Locate every blood parasite and identify its species.
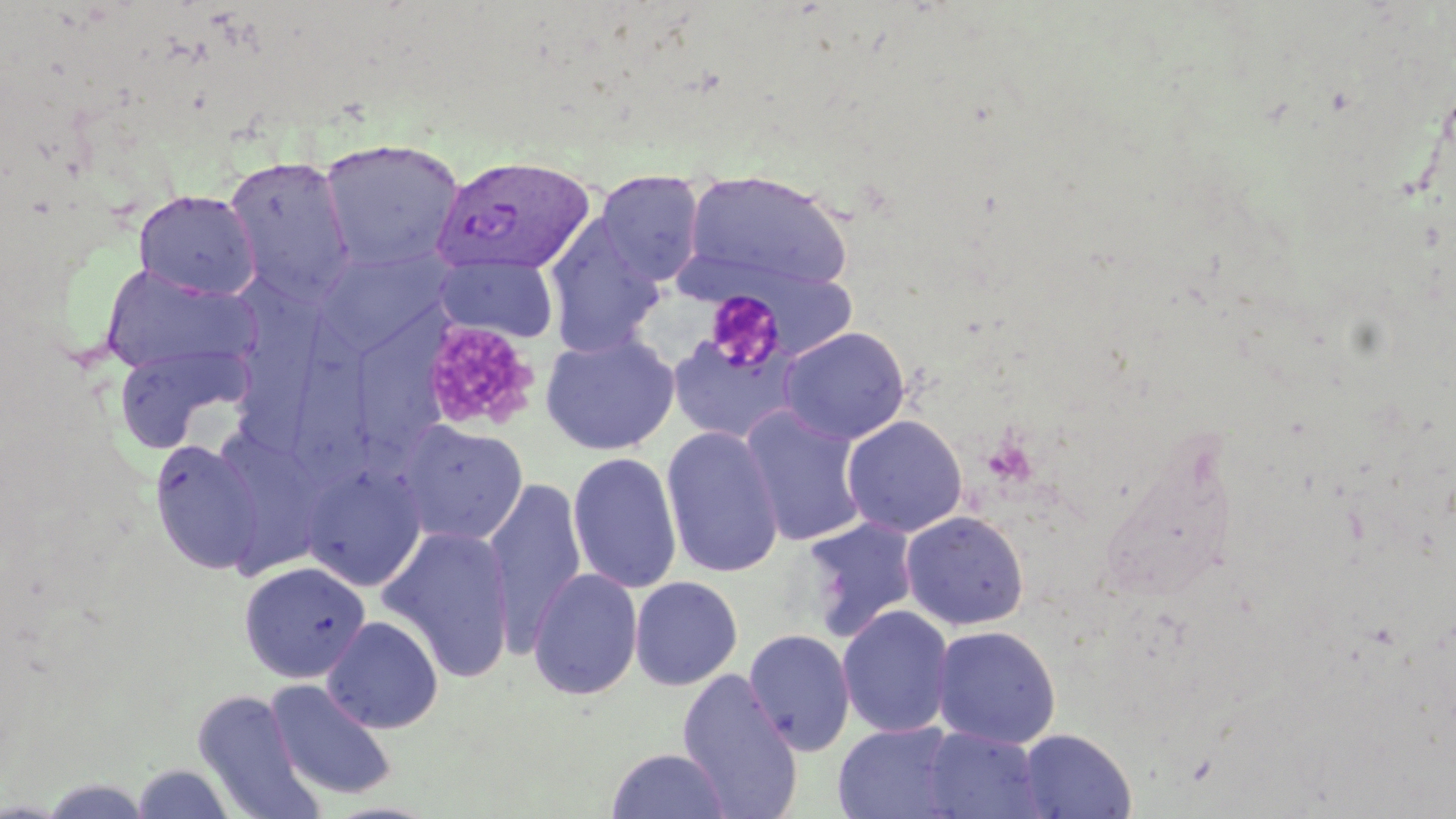

Approximate bounding boxes as named x1/y1/x2/y2 corners in pixels.
Plasmodium vivax-infected red blood cells: (x1=431, y1=155, x2=597, y2=278).
No Plasmodium falciparum, Plasmodium ovale, Plasmodium malariae, Babesia divergens, or Trypanosoma brucei observed.

Platelet locations: (x1=704, y1=289, x2=787, y2=373), (x1=418, y1=320, x2=542, y2=437). Uninfected red blood cell locations: (x1=319, y1=137, x2=465, y2=272), (x1=223, y1=157, x2=357, y2=302), (x1=681, y1=168, x2=855, y2=298), (x1=595, y1=170, x2=706, y2=286), (x1=133, y1=190, x2=261, y2=301), (x1=543, y1=218, x2=666, y2=357), (x1=315, y1=247, x2=454, y2=356), (x1=434, y1=255, x2=561, y2=343), (x1=99, y1=265, x2=258, y2=378), (x1=232, y1=279, x2=326, y2=464), (x1=359, y1=305, x2=445, y2=481), (x1=292, y1=320, x2=385, y2=486), (x1=779, y1=326, x2=911, y2=445), (x1=666, y1=328, x2=805, y2=445), (x1=539, y1=331, x2=680, y2=456), (x1=113, y1=344, x2=250, y2=453), (x1=740, y1=406, x2=870, y2=547), (x1=841, y1=415, x2=968, y2=537), (x1=395, y1=420, x2=529, y2=545), (x1=661, y1=426, x2=784, y2=579), (x1=221, y1=436, x2=323, y2=591), (x1=150, y1=439, x2=264, y2=575), (x1=567, y1=451, x2=682, y2=594), (x1=301, y1=463, x2=427, y2=591), (x1=483, y1=477, x2=588, y2=650), (x1=900, y1=510, x2=1030, y2=631), (x1=800, y1=516, x2=919, y2=642), (x1=379, y1=524, x2=518, y2=683), (x1=238, y1=561, x2=371, y2=684), (x1=528, y1=568, x2=643, y2=701), (x1=629, y1=576, x2=743, y2=690), (x1=837, y1=605, x2=955, y2=738), (x1=322, y1=615, x2=444, y2=734), (x1=930, y1=624, x2=1062, y2=748), (x1=743, y1=628, x2=856, y2=756), (x1=676, y1=668, x2=804, y2=819), (x1=265, y1=679, x2=397, y2=801), (x1=192, y1=691, x2=323, y2=818), (x1=833, y1=721, x2=962, y2=818), (x1=921, y1=726, x2=1046, y2=818), (x1=1017, y1=728, x2=1137, y2=819), (x1=605, y1=747, x2=732, y2=819), (x1=130, y1=763, x2=238, y2=819). Slide-level diagnosis: Plasmodium vivax. Image is 1456×819 pixels. May-Grünwald-Giemsa-stained preparation. One field of a larger specimen. 1000x magnification. Thin blood smear. Optical microscopy.